Classify this cell by malaria status.
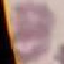
Uninfected.

preparation = thin smear
image type = automatically extracted cell patch, resized to 64 × 64 pixels
stain = Giemsa
capture = smartphone through the microscope eyepiece